Identify the cell.
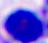

A leukocyte.

Summary:
  - Magnification: 400x
  - Modality: micrograph